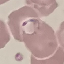
Malaria status: parasitized. Acquired by smartphone through the microscope eyepiece. Giemsa stain. Cell patch, automatically extracted from a larger field of view and resized to 64 × 64 pixels. Thin blood smear.